Assess this cell for malaria.
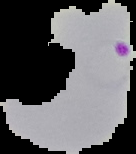

Parasitized.

Image is 136×154 pixels. Cell region segmented out of the field of view; the surrounding area is masked to black. From a thin blood smear.